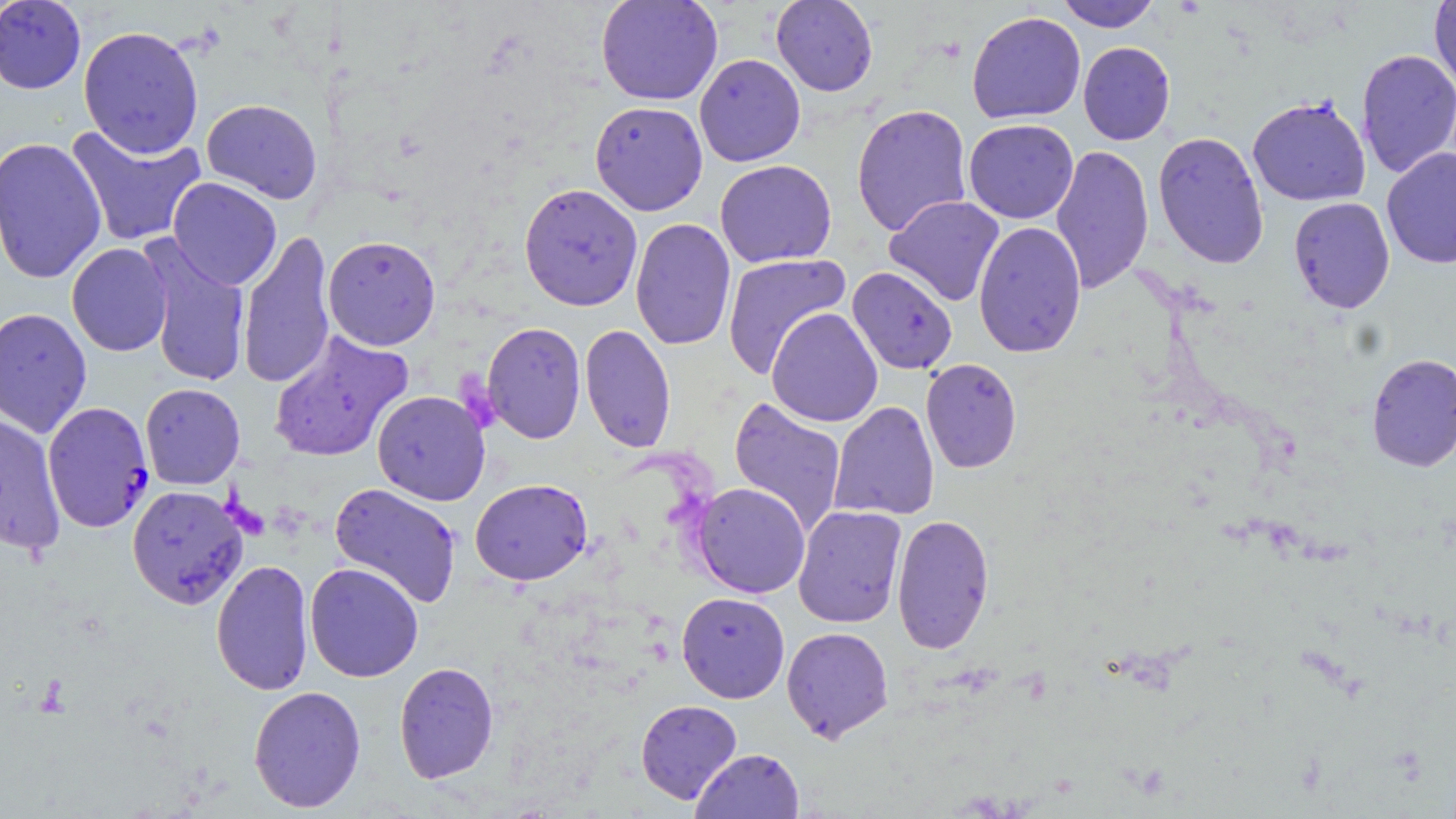
Plasmodium falciparum-infected red blood cell locations = approximate bounding boxes as (x1,y1)-(x2,y2) corner pairs in pixels: (42,402)-(154,533)
slide-level diagnosis = Plasmodium falciparum
magnification = 1000x
image size = 1456×819 pixels
stain = May-Grünwald-Giemsa
modality = light microscopy
field of view = one of a larger specimen
uninfected red blood cell locations = approximate bounding boxes as (x1,y1)-(x2,y2) corner pairs in pixels: (0,0)-(86,94), (596,0)-(723,106), (770,0)-(878,96), (1056,0)-(1160,32), (1429,0)-(1456,93), (967,11)-(1086,124), (78,25)-(204,158), (1078,42)-(1175,145), (1355,48)-(1456,178), (694,53)-(806,167), (1247,96)-(1370,206), (201,99)-(323,203), (590,100)-(708,215), (851,104)-(973,237), (963,118)-(1078,224), (65,123)-(207,248), (1152,131)-(1269,269), (0,136)-(107,284), (1050,144)-(1153,294), (1381,147)-(1456,268), (715,160)-(837,268), (167,177)-(281,290), (519,183)-(643,311), (884,195)-(1005,306), (1289,197)-(1394,314), (630,217)-(736,351), (973,221)-(1087,358), (237,229)-(336,389), (322,235)-(441,350), (138,237)-(252,388), (66,243)-(173,356), (722,253)-(850,378), (847,266)-(958,374), (0,307)-(92,438), (766,307)-(883,427), (481,322)-(586,444), (580,324)-(677,453), (268,330)-(414,462), (1366,353)-(1456,473), (921,357)-(1022,473), (140,383)-(245,489), (372,390)-(490,506), (728,396)-(847,536), (829,401)-(940,520), (0,413)-(66,557), (470,478)-(593,585), (692,482)-(810,598), (329,483)-(462,608), (127,484)-(248,610), (792,505)-(907,628), (891,513)-(995,654), (211,559)-(314,697), (304,562)-(424,682), (676,591)-(790,703), (781,626)-(894,743), (394,661)-(499,783), (248,685)-(366,812), (635,699)-(742,804), (691,748)-(804,819)
preparation = thin blood smear